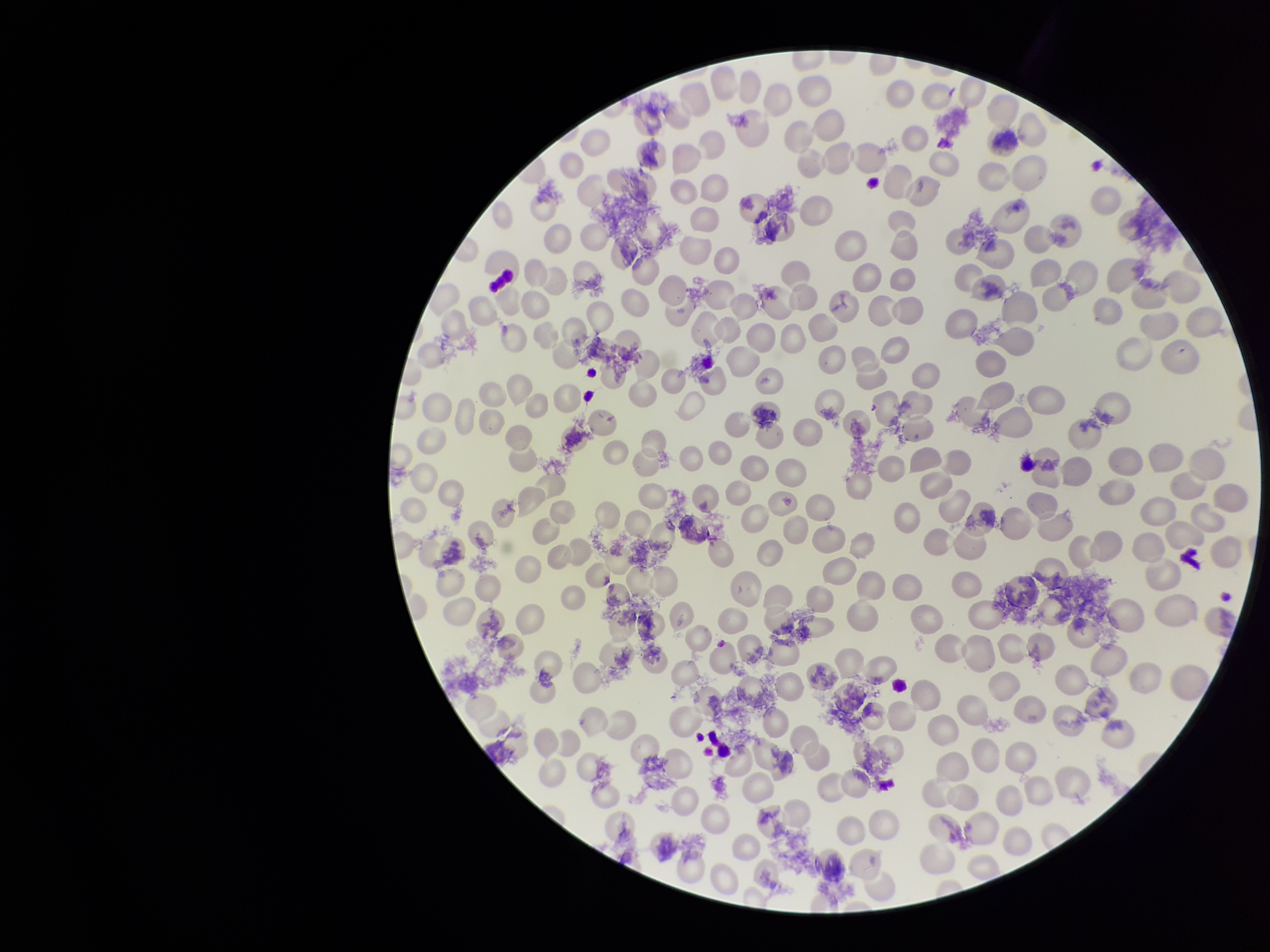
Summary:
  - Parasitized red blood cell count: 0
  - Patient malaria status: negative
  - Image size: 1270×952 pixels
  - Red blood cell count: 221
  - Preparation: thin smear
  - Parasitized red blood cells: none detected
  - Field of view: one from this slide
  - Capture: smartphone photograph through the microscope eyepiece
  - Stain: Giemsa